Identify the parasite.
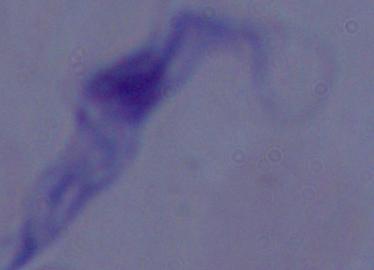
A trypanosome.

{
  "modality": "photomicrograph",
  "magnification": "1000x"
}